Assess the morphology of the red blood cells.
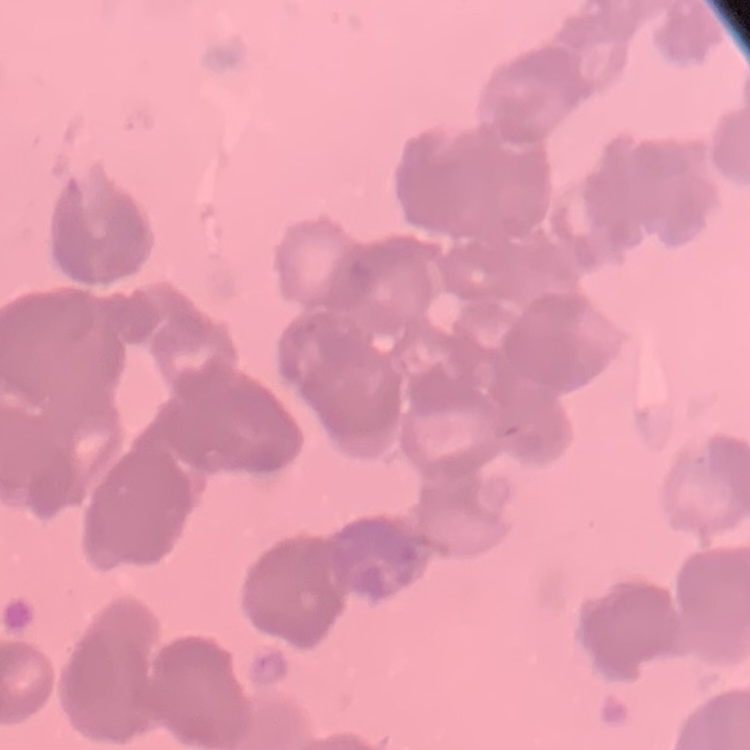

Rouleaux formation.

stain = Field's or Giemsa
image type = one tile cut from a larger photomicrograph
preparation = thin blood smear